Give the position of every Plasmodium parasite visible.
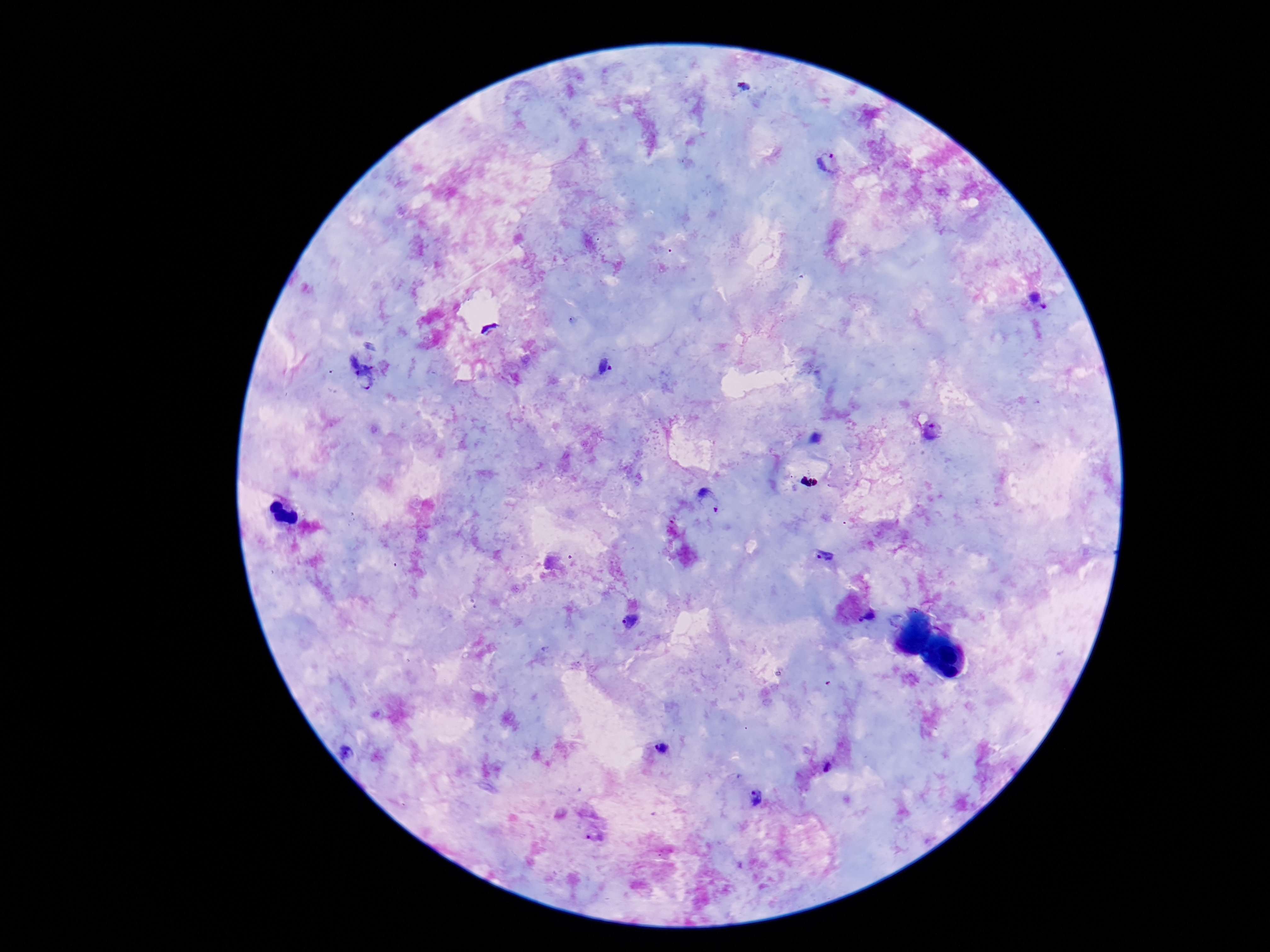
Approximate centers as (x, y) in pixels.
Plasmodium parasites: (832, 163), (1039, 302), (604, 368), (359, 371), (932, 433), (709, 502), (824, 557), (868, 618), (629, 621), (663, 748), (347, 754), (827, 767), (756, 797), (594, 834).

Patient malaria status: positive. Image is 1270×952 pixels. Thick peripheral-blood smear. Single field of view. Giemsa-stained preparation. Photographed through the microscope eyepiece with a smartphone camera. 100x magnification.